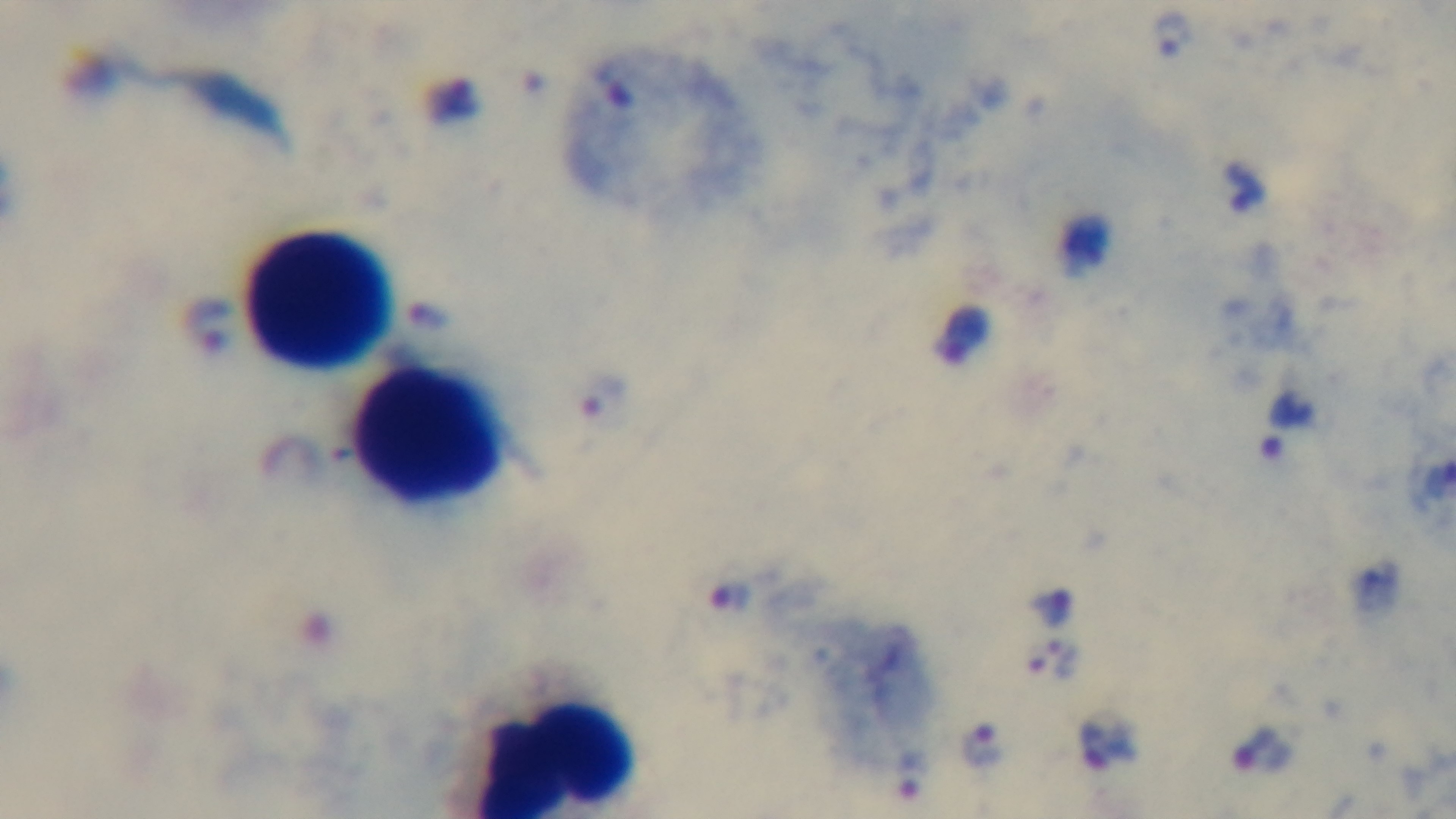
Mounted 4K digital camera. Single field of view. Malaria status: positive. Giemsa-stained. Preparation: thick blood film. Light microscopy. 100x oil-immersion objective.